Assess this cell for malaria.
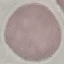

It is uninfected.

stain = Giemsa
preparation = thin smear
image type = automatically extracted cell patch, resized to 64 × 64 pixels
capture = smartphone camera at the microscope eyepiece